Classify this cell by malaria status.
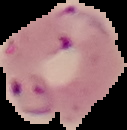

Parasitized.

Summary:
  - Image type: segmented cell region on a black background
  - Image size: 127×130 pixels
  - Preparation: thin blood film